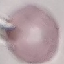

Summary:
  - Result: negative for malaria parasites
  - Capture: smartphone through the microscope eyepiece
  - Preparation: thin blood smear
  - Image type: cell patch, automatically extracted from a larger field of view and resized to 64 × 64 pixels
  - Stain: Giemsa